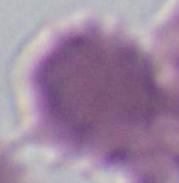

Summary:
  - Identification: red blood cell
  - Magnification: 1000x
  - Modality: photomicrograph